State the blood parasite species.
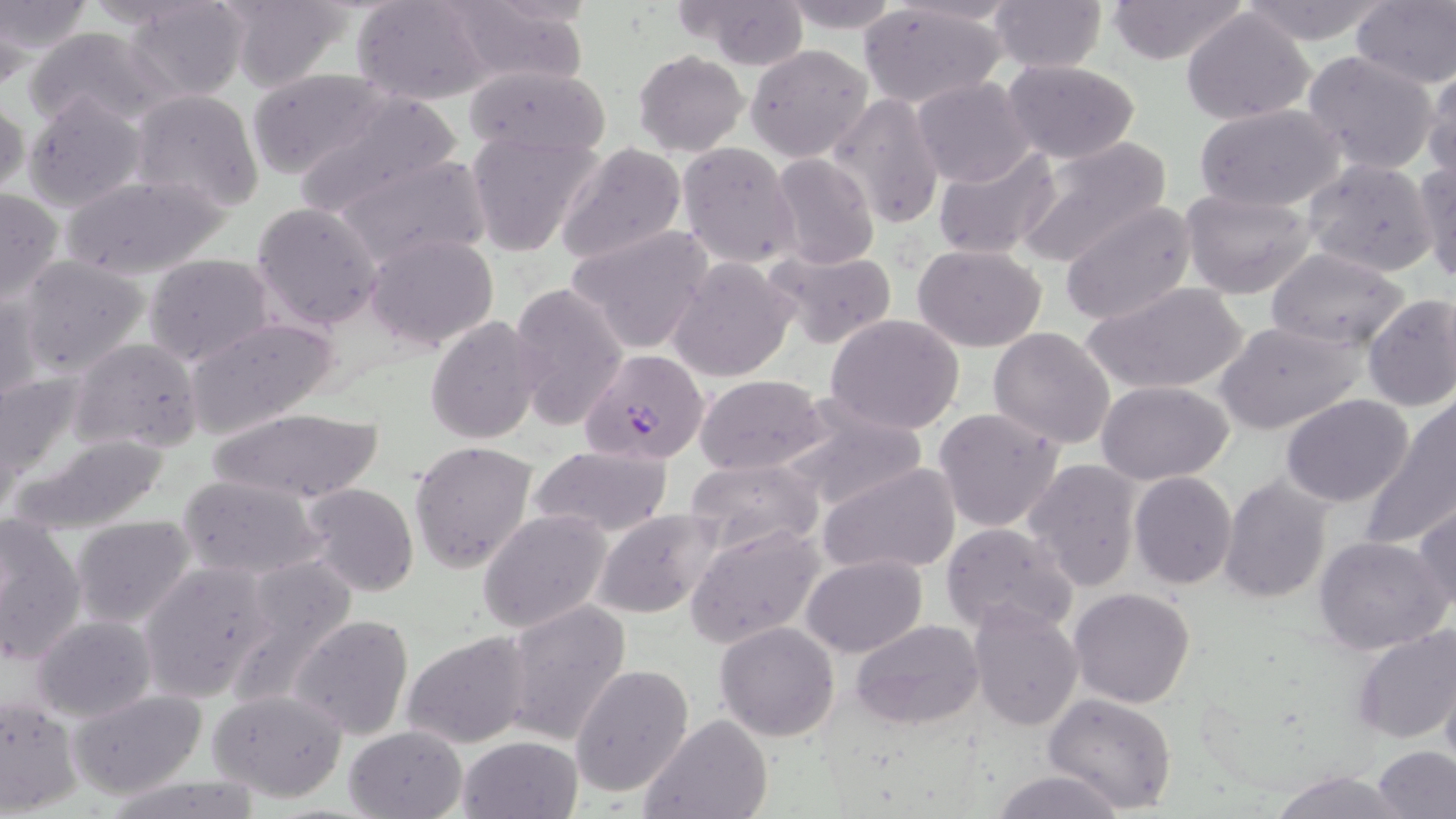

Plasmodium falciparum.

Approximate bounding boxes as [x1, y1, x2, y2] in pixels. Plasmodium falciparum-infected red blood cell locations: [578, 349, 711, 466]. Uninfected red blood cell locations: [218, 0, 353, 92], [352, 0, 494, 106], [677, 0, 814, 70], [779, 0, 902, 34], [1103, 0, 1251, 65], [1237, 0, 1389, 45], [0, 1, 94, 56], [124, 1, 253, 102], [439, 1, 592, 87], [989, 2, 1106, 73], [1351, 2, 1456, 89], [859, 4, 1010, 111], [1180, 8, 1317, 126], [24, 26, 167, 129], [745, 43, 875, 163], [633, 50, 748, 156], [1302, 50, 1441, 176], [1003, 59, 1143, 163], [1423, 63, 1456, 184], [462, 65, 610, 158], [245, 68, 392, 180], [911, 76, 1035, 188], [24, 90, 147, 210], [129, 90, 264, 214], [289, 92, 462, 219], [0, 93, 28, 202], [829, 94, 944, 231], [1193, 104, 1346, 211], [467, 127, 602, 257], [1013, 136, 1170, 269], [676, 142, 800, 268], [554, 143, 689, 266], [932, 146, 1060, 261], [336, 153, 491, 269], [770, 153, 878, 271], [1415, 158, 1456, 282], [1301, 159, 1438, 277], [58, 173, 233, 284], [0, 188, 65, 306], [1181, 189, 1317, 297], [251, 201, 384, 331], [1057, 203, 1195, 327], [567, 223, 713, 357], [364, 231, 500, 352], [913, 244, 1046, 351], [764, 247, 898, 349], [1263, 247, 1411, 352], [143, 253, 276, 367], [17, 255, 151, 377], [667, 256, 798, 382], [508, 281, 630, 434], [1086, 281, 1252, 395], [1, 289, 45, 407], [1360, 293, 1456, 410], [825, 313, 965, 435], [184, 315, 341, 440], [424, 315, 544, 445], [1216, 320, 1366, 434], [987, 327, 1115, 449], [69, 337, 203, 455], [0, 370, 88, 486], [695, 374, 825, 475], [1097, 380, 1234, 484], [1281, 394, 1415, 507], [776, 395, 928, 515], [1366, 397, 1456, 550], [206, 406, 389, 505], [933, 407, 1065, 533], [10, 432, 175, 534], [409, 439, 539, 576], [529, 446, 673, 536], [685, 457, 823, 557], [1023, 460, 1142, 592], [819, 462, 961, 576], [1129, 472, 1237, 589], [176, 474, 324, 579], [1217, 474, 1335, 603], [299, 482, 420, 598], [815, 487, 948, 646], [1412, 501, 1456, 616], [594, 509, 723, 619], [479, 510, 613, 633], [0, 514, 86, 663], [69, 515, 195, 627], [941, 522, 1075, 636], [684, 525, 822, 647], [1313, 535, 1452, 656], [800, 554, 927, 656], [139, 561, 275, 703], [1069, 587, 1195, 709], [969, 599, 1083, 733], [500, 601, 633, 748], [289, 613, 415, 742], [31, 615, 156, 721], [849, 618, 984, 732], [715, 622, 839, 740], [1350, 626, 1456, 743], [400, 631, 532, 749], [570, 663, 693, 798], [1441, 668, 1456, 775], [207, 688, 350, 801], [69, 689, 207, 799], [0, 693, 83, 816], [1043, 694, 1178, 814], [641, 715, 772, 819], [344, 724, 468, 818], [458, 735, 583, 819], [1372, 745, 1455, 819], [990, 769, 1131, 819], [1267, 770, 1405, 818], [99, 772, 266, 819]. Light microscopy. Image is 1456×819 pixels. Captured at 1000x magnification. One field of a larger specimen. Thin blood film. May-Grünwald-Giemsa stain.